Describe the morphology of the erythrocytes.
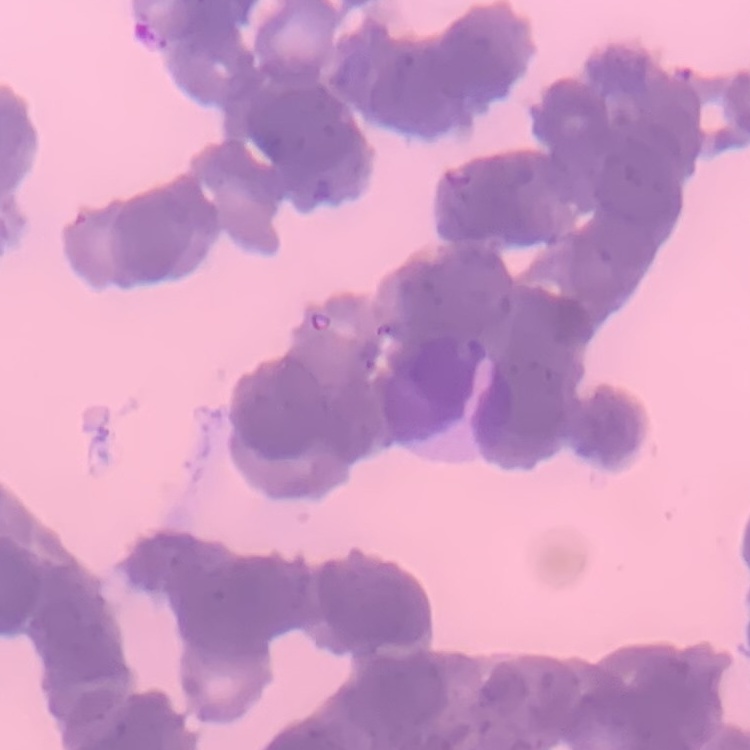

They show rouleaux formation.

Summary:
  - Stain: Field's or Giemsa
  - Image type: one tile cut from a larger photomicrograph
  - Preparation: thin blood smear